Name the cell type shown.
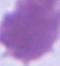

This is an erythrocyte.

Captured at 1000x magnification. Micrograph.